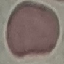
Summary:
  - Result: negative for malaria parasites
  - Stain: Giemsa
  - Image type: cell patch, automatically extracted from a larger field of view and resized to 64 × 64 pixels
  - Capture: smartphone camera at the microscope eyepiece
  - Preparation: thin blood film